Report the malaria status of this cell.
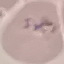
It is parasitized.

preparation = thin blood film
stain = Giemsa
image type = automatically extracted cell patch, resized to 64 × 64 pixels
capture = smartphone camera at the microscope eyepiece